Locate and identify every blood parasite.
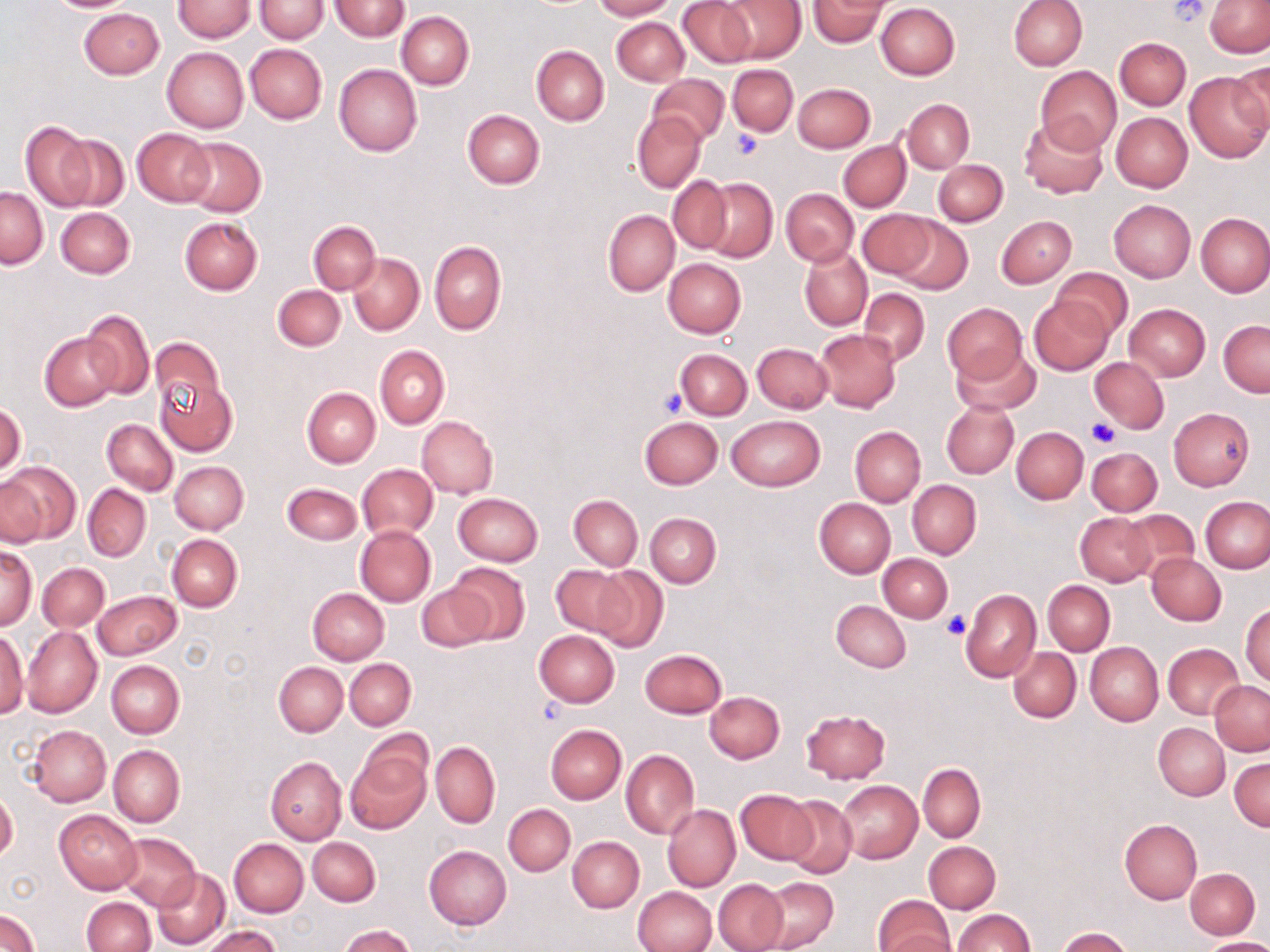

No blood parasites observed.

Summary:
  - Coordinate format: approximate bounding boxes as [x1, y1, x2, y2] in pixels
  - Uninfected red blood cell locations: [44, 0, 139, 13], [173, 0, 254, 41], [592, 0, 675, 20], [677, 0, 757, 68], [809, 0, 888, 47], [1008, 0, 1086, 71], [1205, 0, 1270, 57], [255, 1, 328, 42], [331, 1, 409, 41], [718, 1, 807, 63], [875, 3, 959, 80], [79, 7, 164, 79], [397, 12, 474, 89], [612, 18, 688, 85], [1115, 37, 1191, 110], [246, 44, 327, 124], [531, 46, 609, 125], [161, 47, 248, 133], [1230, 61, 1270, 142], [334, 64, 422, 157], [728, 64, 797, 136], [1036, 67, 1122, 152], [1185, 71, 1270, 162], [648, 73, 729, 146], [792, 82, 875, 153], [903, 99, 974, 173], [463, 109, 545, 189], [1111, 112, 1193, 192], [633, 113, 705, 192], [1019, 115, 1108, 199], [20, 120, 97, 210], [132, 129, 215, 206], [53, 133, 129, 211], [180, 137, 265, 217], [838, 140, 910, 212], [933, 160, 1007, 226], [668, 175, 732, 255], [698, 177, 778, 262], [1, 187, 47, 268], [781, 188, 859, 267], [1108, 200, 1195, 283], [56, 207, 135, 279], [603, 210, 679, 295], [857, 210, 935, 280], [1196, 213, 1270, 297], [997, 215, 1076, 287], [891, 216, 972, 294], [180, 217, 263, 295], [308, 221, 380, 294], [429, 241, 507, 335], [800, 248, 872, 331], [348, 253, 424, 335], [663, 257, 746, 337], [1053, 267, 1132, 341], [273, 285, 345, 351], [858, 288, 930, 365], [1028, 295, 1113, 375], [1124, 303, 1211, 381], [942, 304, 1028, 383], [84, 310, 154, 399], [1219, 319, 1269, 397], [816, 329, 901, 413], [40, 333, 122, 411], [149, 336, 226, 419], [752, 343, 832, 413], [952, 344, 1039, 415], [375, 345, 449, 428], [675, 349, 751, 419], [1090, 357, 1169, 432], [156, 377, 238, 457], [302, 386, 380, 468], [942, 401, 1018, 478], [0, 403, 25, 477], [1168, 407, 1253, 491], [727, 415, 824, 491], [417, 416, 498, 499], [638, 416, 723, 490], [102, 419, 178, 495], [850, 426, 925, 506], [1012, 427, 1088, 503], [1087, 448, 1161, 516], [170, 461, 248, 534], [3, 463, 79, 544], [358, 465, 438, 540], [0, 476, 45, 547], [907, 481, 982, 559], [282, 483, 362, 544], [83, 484, 151, 561], [452, 492, 543, 566], [569, 495, 643, 569], [1201, 496, 1269, 573], [814, 497, 895, 578], [1120, 509, 1201, 586], [1075, 512, 1154, 586], [646, 513, 721, 587], [355, 526, 435, 605], [166, 534, 242, 611], [0, 546, 37, 631], [879, 553, 953, 622], [1148, 553, 1225, 626], [38, 564, 109, 632], [447, 564, 529, 643], [550, 564, 635, 637], [591, 565, 668, 652], [1043, 580, 1114, 655], [417, 583, 494, 652], [308, 588, 389, 664], [962, 588, 1041, 682], [93, 590, 180, 660], [832, 599, 911, 671], [1241, 602, 1269, 686], [20, 625, 102, 718], [0, 630, 28, 719], [533, 630, 619, 707], [1085, 642, 1162, 725], [1164, 643, 1243, 719], [640, 648, 727, 718], [1009, 648, 1080, 722], [345, 658, 415, 729], [106, 660, 185, 737], [274, 661, 348, 737], [1209, 682, 1270, 755], [705, 691, 784, 762], [800, 708, 891, 783], [1154, 723, 1230, 799], [28, 724, 110, 807], [545, 724, 626, 803], [430, 742, 499, 827], [108, 745, 185, 826], [345, 746, 431, 834], [621, 749, 700, 838], [265, 756, 346, 845], [1229, 756, 1270, 831], [918, 763, 985, 843], [836, 780, 922, 864], [0, 788, 18, 864], [736, 789, 819, 864], [781, 796, 858, 879], [504, 804, 575, 876], [662, 804, 741, 891], [54, 810, 142, 894], [1120, 818, 1202, 905], [115, 833, 201, 909], [568, 836, 644, 912], [308, 837, 381, 906], [228, 839, 308, 917], [925, 840, 1000, 914], [423, 844, 511, 929], [1186, 868, 1260, 938], [152, 869, 231, 948], [759, 877, 838, 952], [713, 878, 789, 952], [631, 887, 717, 952], [873, 896, 954, 952], [82, 897, 154, 951], [953, 909, 1034, 952], [0, 910, 41, 951], [339, 925, 416, 952], [202, 926, 280, 952], [1057, 928, 1135, 952], [877, 933, 959, 952], [1202, 938, 1270, 952]
  - Platelet locations: [1169, 0, 1212, 25], [733, 130, 764, 158], [657, 385, 688, 418], [1086, 419, 1117, 446], [942, 613, 968, 639]
  - Slide-level diagnosis: negative for blood parasites
  - Image size: 1270×952 pixels
  - Preparation: thin blood film
  - Field of view: one of a larger specimen
  - Modality: optical microscopy
  - Magnification: 1000x
  - Stain: May-Grünwald-Giemsa